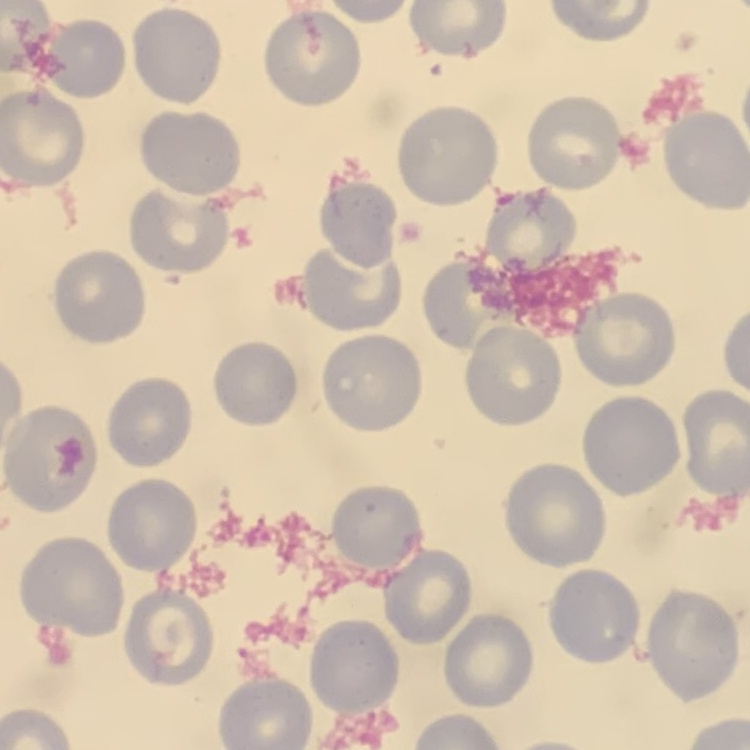
red_blood_cell_morphology: no rouleaux formation
image_type: square crop of a larger photomicrograph
preparation: thin blood film
stain: Field's or Giemsa